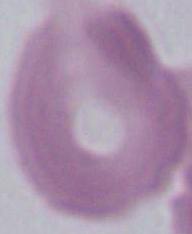

magnification = 1000x
modality = micrograph
identification = erythrocyte